Comment on the morphology of the red blood cells.
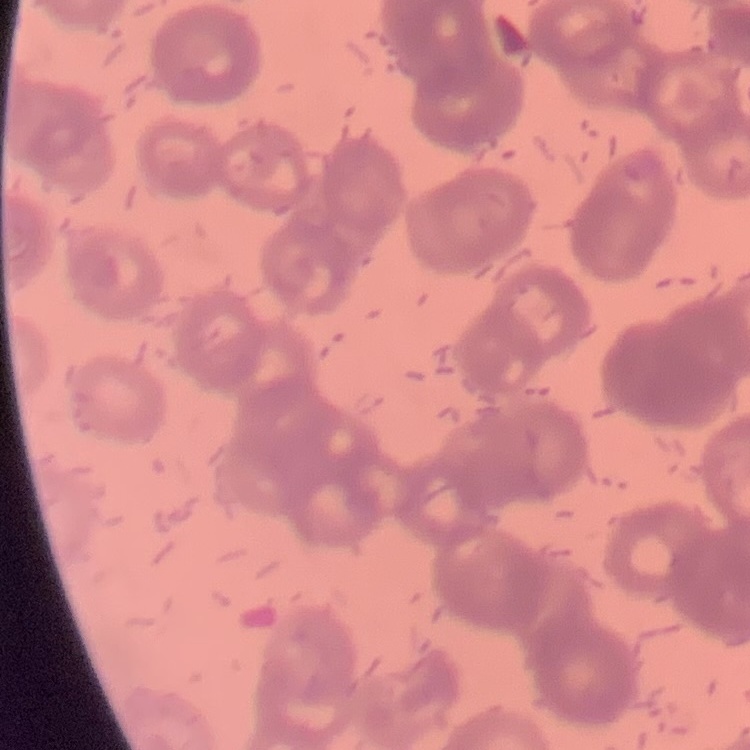

They show rouleaux formation.

Stained with either Field's or Giemsa. One tile cut from a larger photomicrograph. Thin blood smear.